Classify this cell by malaria status.
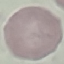
Uninfected.

Giemsa stain. Acquired by smartphone through the microscope eyepiece. Cell patch, automatically extracted from a larger field of view and resized to 64 × 64 pixels. Thin smear of blood.